Locate every Plasmodium malariae-infected red blood cell.
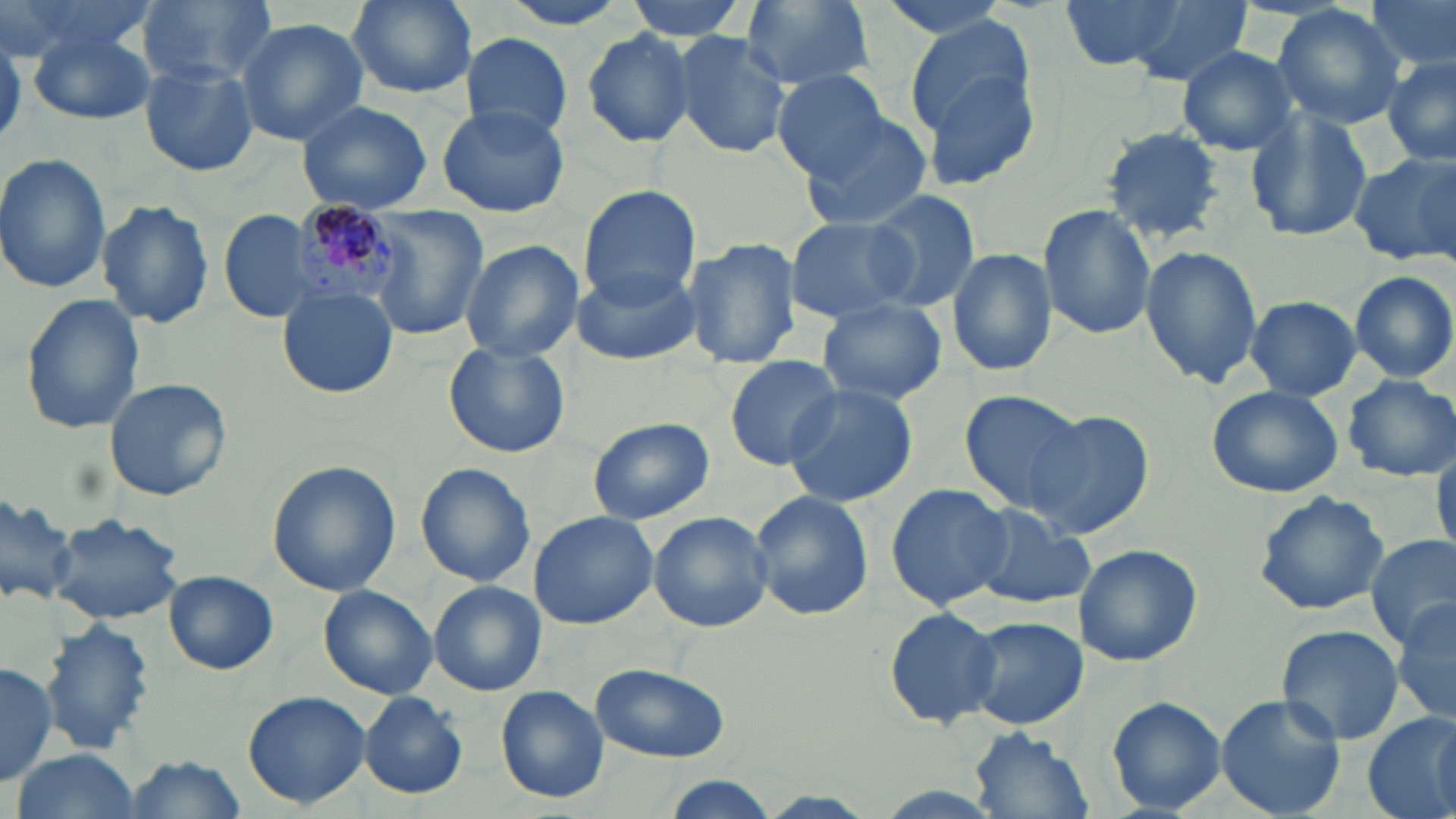

Approximate bounding boxes as (x1, y1, x2, y2) in pixels.
Plasmodium malariae-infected red blood cells: (291, 197, 400, 305).

slide-level diagnosis = Plasmodium malariae
image size = 1456×819 pixels
preparation = thin blood smear
modality = optical microscopy
stain = May-Grünwald-Giemsa
magnification = 1000x
uninfected red blood cell locations = approximate bounding boxes as (x1, y1, x2, y2) in pixels: (3, 0, 160, 66), (138, 0, 274, 86), (492, 0, 638, 32), (621, 0, 753, 40), (738, 0, 877, 94), (872, 0, 1019, 41), (1059, 0, 1185, 72), (1365, 0, 1455, 76), (345, 1, 478, 99), (1117, 2, 1252, 87), (1270, 4, 1407, 130), (236, 18, 368, 144), (905, 20, 1043, 190), (26, 28, 157, 125), (580, 28, 698, 147), (670, 32, 793, 160), (458, 33, 575, 140), (1176, 44, 1300, 156), (1382, 54, 1456, 167), (140, 62, 259, 177), (771, 70, 895, 179), (294, 98, 436, 213), (437, 104, 570, 218), (797, 108, 936, 230), (1245, 108, 1377, 242), (1096, 125, 1229, 246), (1347, 149, 1456, 266), (0, 153, 112, 293), (577, 185, 703, 309), (863, 190, 981, 313), (96, 200, 215, 328), (1038, 204, 1157, 339), (221, 208, 321, 324), (365, 208, 486, 339), (785, 216, 920, 325), (459, 239, 584, 363), (683, 239, 800, 371), (1140, 242, 1264, 389), (947, 246, 1057, 379), (571, 262, 703, 368), (1349, 270, 1456, 384), (277, 286, 399, 400), (18, 294, 147, 436), (1245, 296, 1361, 400), (816, 297, 949, 405), (444, 341, 570, 458), (724, 356, 843, 468), (1341, 375, 1456, 481), (104, 378, 231, 501), (779, 384, 919, 508), (1207, 384, 1345, 499), (958, 388, 1096, 513), (1025, 410, 1155, 541), (588, 416, 714, 525), (1431, 445, 1456, 559), (267, 460, 400, 598), (414, 462, 536, 586), (886, 483, 1014, 611), (0, 489, 76, 608), (749, 491, 875, 621), (1251, 491, 1390, 615), (966, 505, 1095, 610), (528, 510, 660, 629), (647, 511, 773, 633), (48, 513, 184, 624), (1367, 533, 1456, 648), (1074, 543, 1203, 668), (164, 570, 279, 674), (428, 582, 545, 694), (316, 584, 438, 699), (1390, 600, 1456, 726), (882, 606, 1004, 729), (961, 615, 1088, 732), (39, 617, 154, 758), (1276, 623, 1405, 747), (0, 660, 58, 787), (590, 662, 730, 764), (494, 685, 610, 803), (241, 689, 372, 809), (357, 691, 469, 800), (1216, 694, 1349, 819), (1106, 696, 1228, 815), (1363, 712, 1456, 819), (965, 726, 1092, 819), (11, 749, 141, 819), (118, 754, 250, 819), (661, 778, 779, 819)
field of view = single